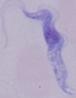

Captured at 1000x magnification. A trypanosome is seen. Photomicrograph.